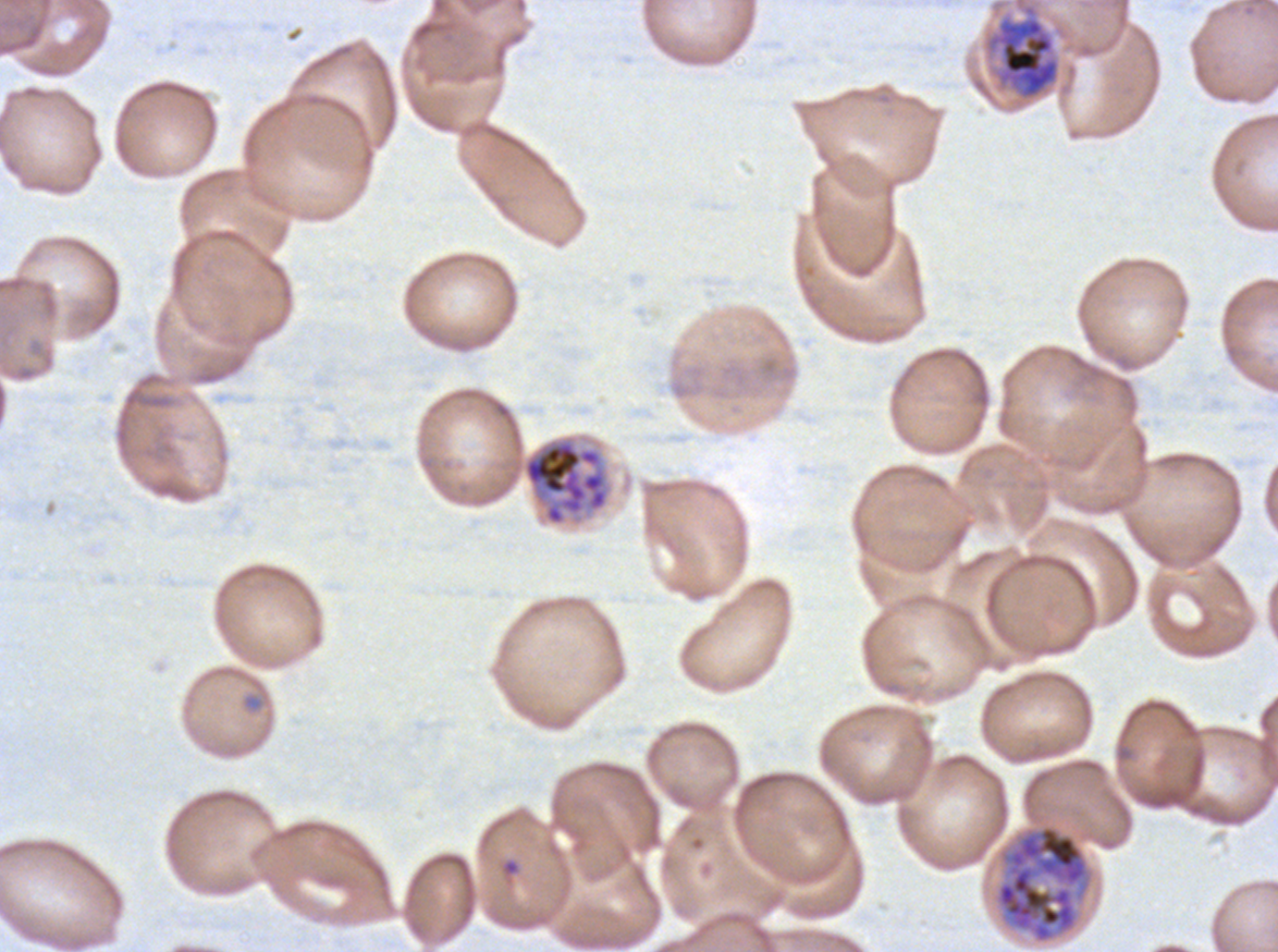
Approximate bounding rectangles given as corner coordinates in pixels from the top-left. Late schizont locations: (x1=522, y1=437, x2=610, y2=526), (x1=994, y1=824, x2=1090, y2=945). Late trophozoite locations: (x1=982, y1=0, x2=1062, y2=103). Ex-vivo Plasmodium falciparum culture from a patient in The Gambia, grown for 24 to 48 hours. Giemsa-stained preparation. Life-cycle stages observed: late trophozoite, late schizont. Image is 1278×952 pixels. Thin blood film. One sub-image of a larger composite.